Name the parasite shown.
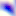
This is Toxoplasma gondii.

magnification = 400x
modality = photomicrograph